Describe the morphology of the erythrocytes.
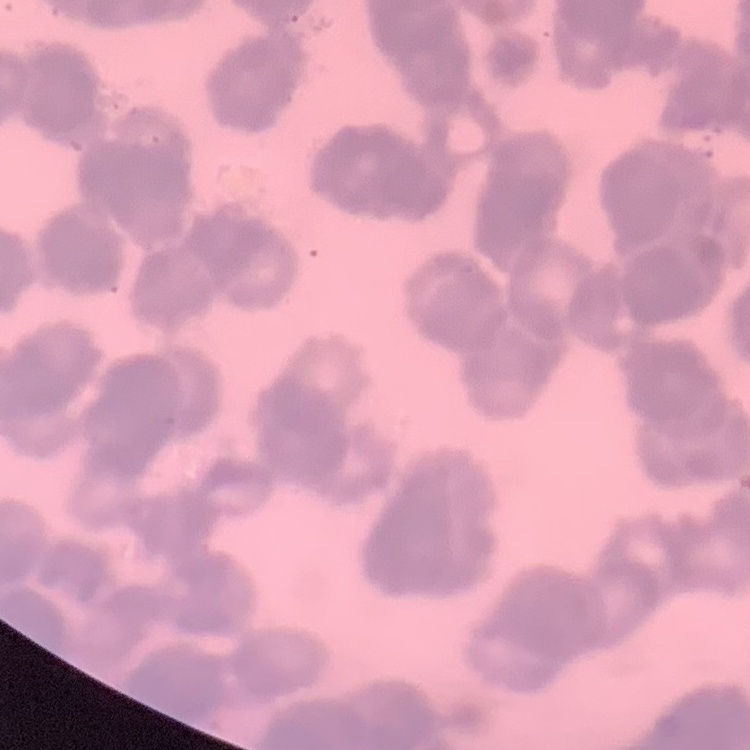
They show rouleaux formation.

preparation = thin peripheral smear
image type = square crop of a larger photomicrograph
stain = Field's or Giemsa